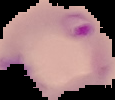 Image is 115×100 pixels. Segmented cell region on a black background. From a thin blood film. Result: malaria parasites detected.